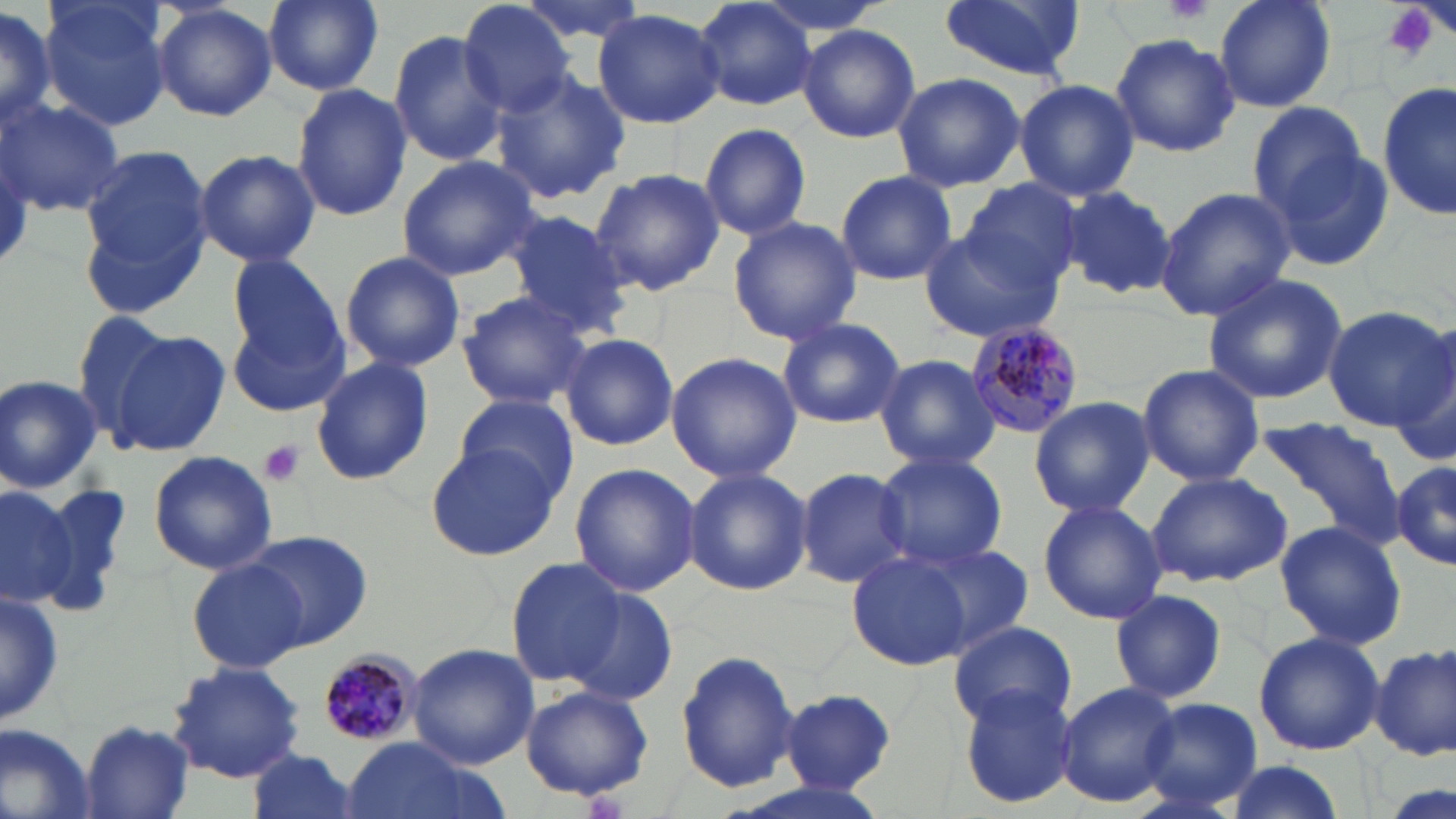
slide_level_diagnosis: Plasmodium malariae
preparation: thin blood film
plasmodium_malariae_infected_red_blood_cell_locations: 'approximate bounding boxes as named x1/y1/x2/y2 corners in pixels: (x1=959, y1=321, x2=1086, y2=435), (x1=316, y1=649, x2=422, y2=749)'
modality: light microscopy
image_size: 1456×819 pixels
platelet_locations: 'approximate bounding boxes as named x1/y1/x2/y2 corners in pixels: (x1=1163, y1=0, x2=1213, y2=25), (x1=1380, y1=2, x2=1442, y2=61), (x1=258, y1=441, x2=306, y2=486)'
field_of_view: single
stain: May-Grünwald-Giemsa
uninfected_red_blood_cell_locations: 'approximate bounding boxes as named x1/y1/x2/y2 corners in pixels: (x1=40, y1=0, x2=173, y2=131), (x1=261, y1=0, x2=387, y2=96), (x1=515, y1=0, x2=651, y2=46), (x1=939, y1=0, x2=1087, y2=81), (x1=1212, y1=0, x2=1337, y2=114), (x1=149, y1=1, x2=278, y2=123), (x1=460, y1=1, x2=579, y2=117), (x1=0, y1=2, x2=58, y2=131), (x1=695, y1=2, x2=816, y2=112), (x1=592, y1=8, x2=726, y2=129), (x1=799, y1=24, x2=920, y2=144), (x1=386, y1=27, x2=512, y2=168), (x1=1109, y1=32, x2=1241, y2=157), (x1=492, y1=71, x2=628, y2=204), (x1=890, y1=71, x2=1026, y2=192), (x1=1014, y1=79, x2=1139, y2=202), (x1=293, y1=82, x2=411, y2=221), (x1=1378, y1=82, x2=1456, y2=219), (x1=2, y1=96, x2=123, y2=217), (x1=1247, y1=102, x2=1373, y2=219), (x1=698, y1=122, x2=811, y2=241), (x1=704, y1=139, x2=831, y2=323), (x1=1270, y1=142, x2=1396, y2=273), (x1=78, y1=143, x2=217, y2=305), (x1=195, y1=149, x2=321, y2=267), (x1=395, y1=154, x2=539, y2=281), (x1=588, y1=167, x2=724, y2=296), (x1=836, y1=169, x2=957, y2=285), (x1=957, y1=177, x2=1087, y2=292), (x1=1060, y1=185, x2=1176, y2=301), (x1=1154, y1=187, x2=1296, y2=322), (x1=502, y1=209, x2=632, y2=339), (x1=727, y1=216, x2=862, y2=345), (x1=919, y1=229, x2=1064, y2=344), (x1=340, y1=252, x2=466, y2=371), (x1=228, y1=255, x2=346, y2=369), (x1=1201, y1=271, x2=1349, y2=406), (x1=456, y1=291, x2=594, y2=411), (x1=1322, y1=304, x2=1456, y2=431), (x1=72, y1=309, x2=184, y2=445), (x1=229, y1=311, x2=347, y2=417), (x1=774, y1=318, x2=908, y2=430), (x1=108, y1=327, x2=230, y2=457), (x1=1387, y1=327, x2=1456, y2=468), (x1=560, y1=333, x2=680, y2=452), (x1=665, y1=351, x2=803, y2=482), (x1=875, y1=353, x2=1000, y2=471), (x1=309, y1=355, x2=434, y2=487), (x1=1136, y1=362, x2=1266, y2=487), (x1=1, y1=375, x2=103, y2=492), (x1=451, y1=393, x2=580, y2=500), (x1=1029, y1=395, x2=1154, y2=516), (x1=1259, y1=418, x2=1405, y2=545), (x1=426, y1=444, x2=560, y2=561), (x1=872, y1=449, x2=1009, y2=570), (x1=147, y1=450, x2=277, y2=575), (x1=1388, y1=459, x2=1456, y2=570), (x1=568, y1=462, x2=701, y2=598), (x1=684, y1=467, x2=813, y2=596), (x1=794, y1=467, x2=912, y2=588), (x1=1148, y1=470, x2=1292, y2=587), (x1=0, y1=482, x2=77, y2=607), (x1=1036, y1=499, x2=1167, y2=626), (x1=1274, y1=520, x2=1408, y2=650), (x1=244, y1=532, x2=373, y2=650), (x1=903, y1=540, x2=1034, y2=661), (x1=841, y1=543, x2=994, y2=667), (x1=504, y1=557, x2=628, y2=690), (x1=187, y1=558, x2=306, y2=673), (x1=567, y1=587, x2=679, y2=706), (x1=1109, y1=587, x2=1227, y2=705), (x1=1, y1=591, x2=65, y2=724), (x1=949, y1=620, x2=1077, y2=729), (x1=1252, y1=631, x2=1386, y2=756), (x1=407, y1=643, x2=539, y2=767), (x1=1371, y1=643, x2=1455, y2=761), (x1=676, y1=649, x2=800, y2=794), (x1=167, y1=662, x2=306, y2=783), (x1=1055, y1=682, x2=1180, y2=808), (x1=520, y1=684, x2=654, y2=802), (x1=957, y1=686, x2=1078, y2=811), (x1=778, y1=688, x2=898, y2=797), (x1=1136, y1=697, x2=1266, y2=813), (x1=80, y1=719, x2=194, y2=819), (x1=0, y1=722, x2=98, y2=819), (x1=340, y1=737, x2=490, y2=819), (x1=245, y1=750, x2=363, y2=819), (x1=1220, y1=760, x2=1348, y2=818), (x1=721, y1=777, x2=897, y2=819)'
magnification: 1000x